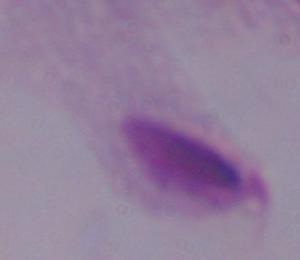
identification: trichomonad
modality: photomicrograph
magnification: 1000x